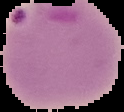

Cell region segmented out of the field of view; the surrounding area is masked to black. From a thin blood smear. Image is 124×112 pixels. Malaria status: parasitized.